Assess this cell for malaria.
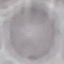

Uninfected.

{
  "image_type": "cell patch, automatically extracted from a larger field of view and resized to 64 × 64 pixels",
  "capture": "smartphone camera at the microscope eyepiece",
  "preparation": "thin blood smear",
  "stain": "Giemsa"
}